Comment on the morphology of the red blood cells.
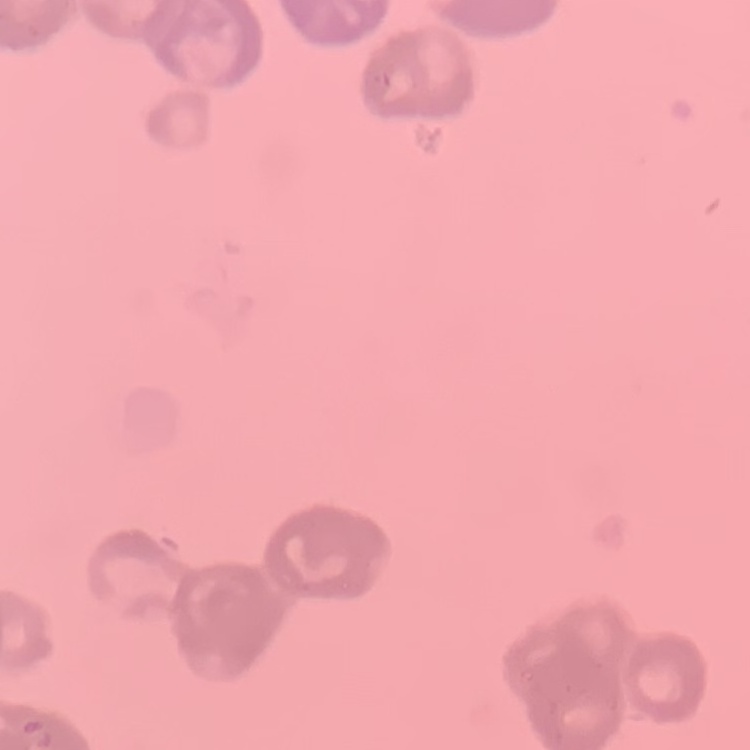

They show rouleaux formation.

Summary:
  - Image type: one tile cut from a larger photomicrograph
  - Preparation: thin peripheral smear
  - Stain: Field's or Giemsa